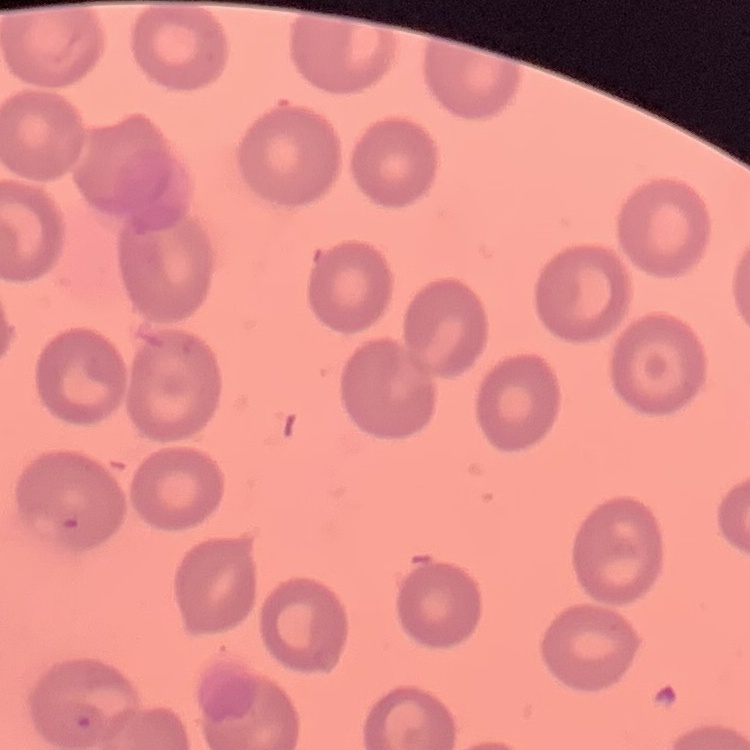 The erythrocytes show no rouleaux formation. One tile cut from a larger photomicrograph. Field's or Giemsa stain. Thin blood film.